State which parasite is depicted.
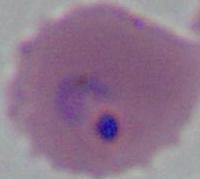
Plasmodium.

magnification = 400x or 1000x
modality = photomicrograph